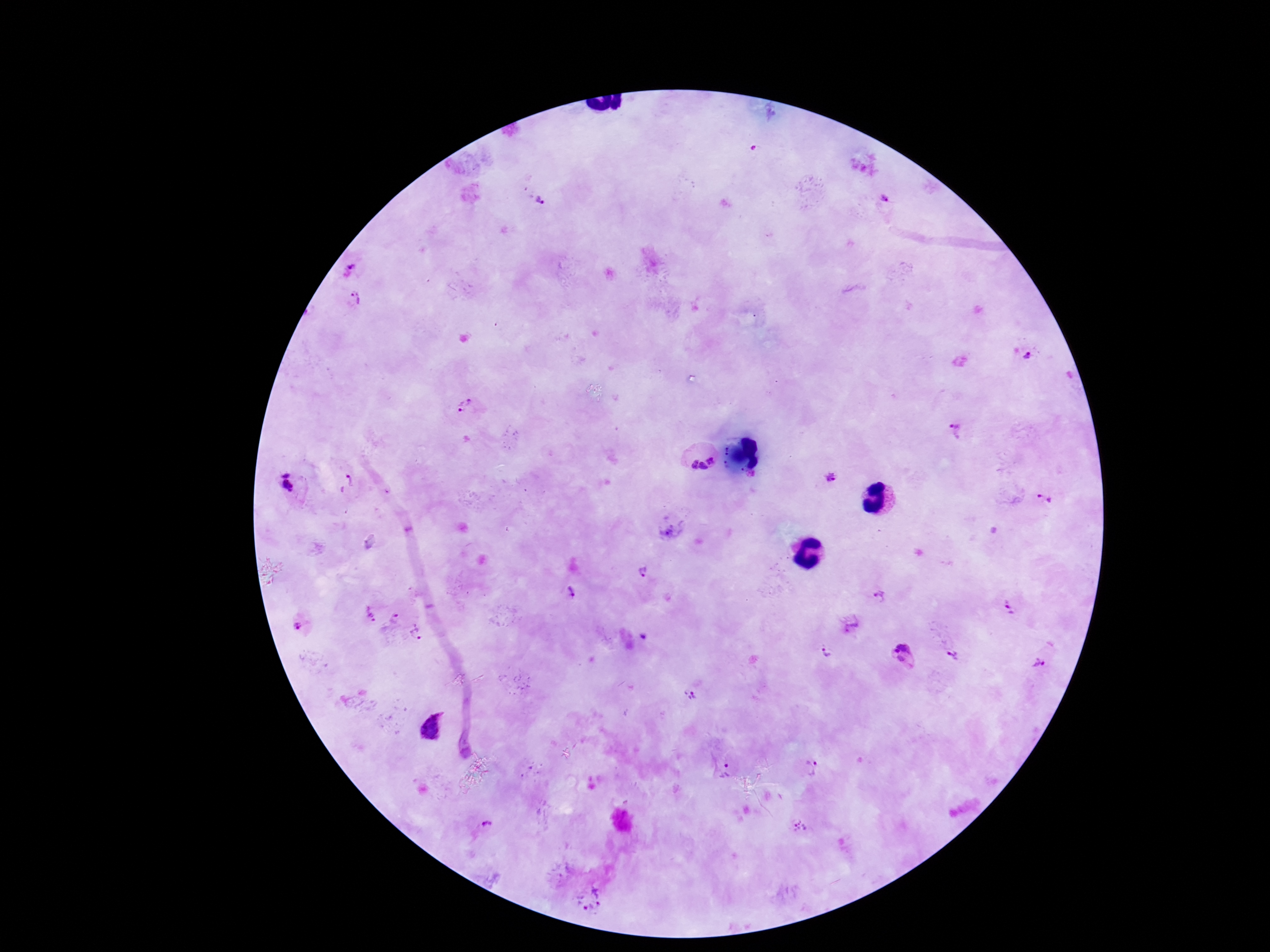 Approximate object centers, in pixels from the top-left corner. Plasmodium parasite locations: (x=754, y=149), (x=539, y=198), (x=887, y=198), (x=348, y=269), (x=354, y=298), (x=1030, y=352), (x=463, y=405), (x=955, y=433), (x=696, y=455), (x=832, y=476), (x=349, y=478), (x=288, y=483), (x=1044, y=497), (x=673, y=528), (x=641, y=572), (x=571, y=591), (x=879, y=597), (x=1008, y=607), (x=369, y=615), (x=396, y=618), (x=298, y=626), (x=853, y=626), (x=418, y=632), (x=828, y=653), (x=903, y=655), (x=954, y=656), (x=1038, y=663), (x=691, y=694), (x=432, y=728), (x=812, y=768), (x=727, y=773), (x=487, y=825), (x=800, y=825), (x=590, y=897). One field from this slide. 100x magnification. Patient malaria status: positive. Giemsa-stained preparation. Smartphone photograph taken through the microscope eyepiece. Image is 1270×952 pixels. Thick peripheral-blood smear.